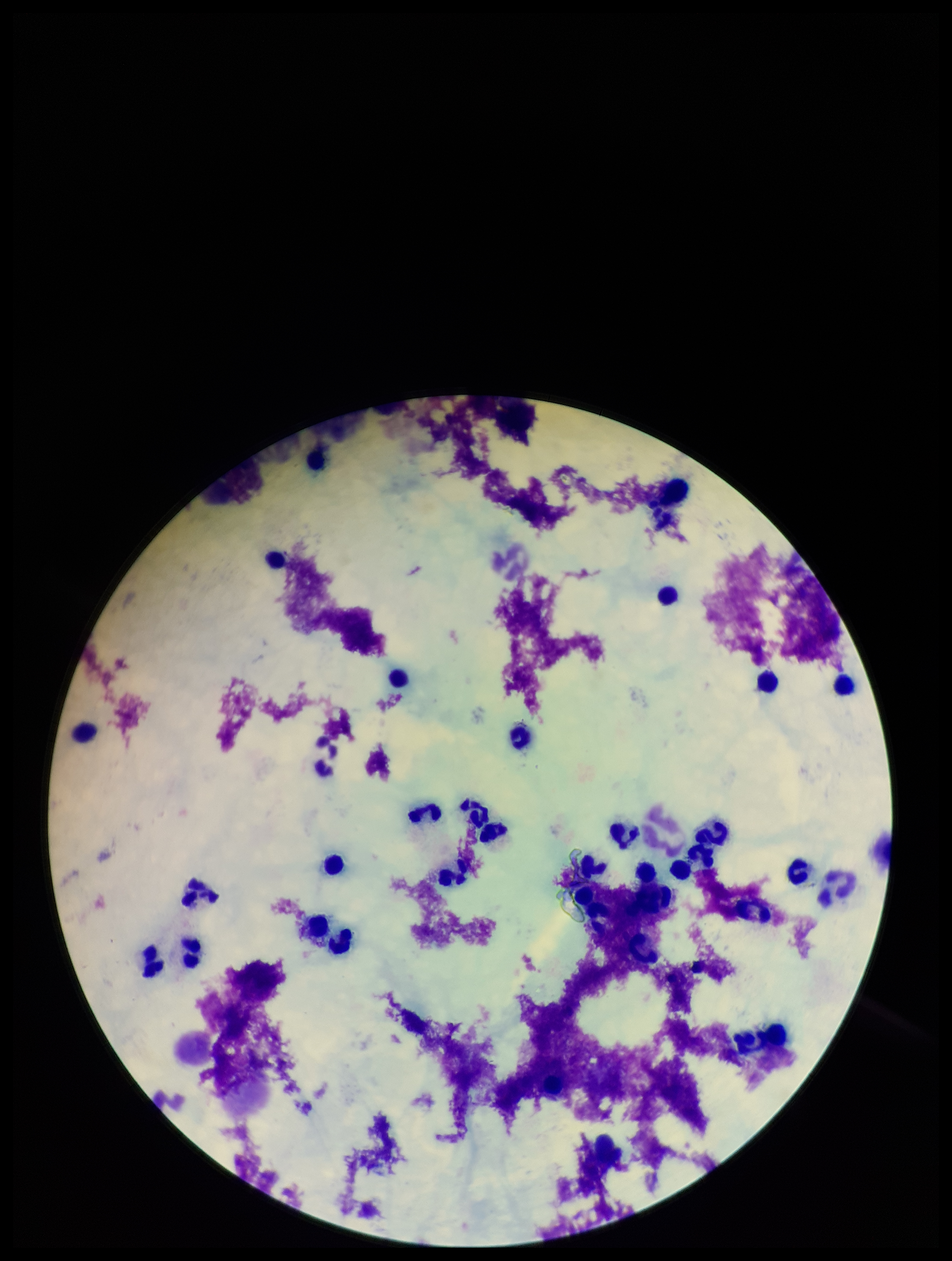

capture = smartphone photograph through the microscope eyepiece
preparation = thick
field of view = one from this slide
parasite count = 0
image size = 952×1261 pixels
patient malaria status = negative
leukocyte count = 32
Plasmodium parasites = none seen
stain = Giemsa